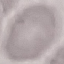
Summary:
  - Malaria status: uninfected
  - Preparation: thin blood smear
  - Capture: smartphone camera at the microscope eyepiece
  - Stain: Giemsa
  - Image type: automatically extracted cell patch, resized to 64 × 64 pixels